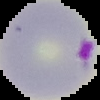
Summary:
  - Image size: 100×100 pixels
  - Result: Plasmodium parasites identified
  - Image type: segmented cell region with the area outside set to black
  - Preparation: thin blood film